Assess this cell for malaria.
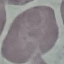

Uninfected.

{
  "image_type": "cell patch, automatically extracted from a larger field of view and resized to 64 × 64 pixels",
  "capture": "smartphone camera at the microscope eyepiece",
  "preparation": "thin blood smear",
  "stain": "Giemsa"
}